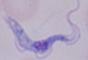
magnification: 1000x
identification: trypanosome
modality: micrograph